Locate and identify every blood parasite.
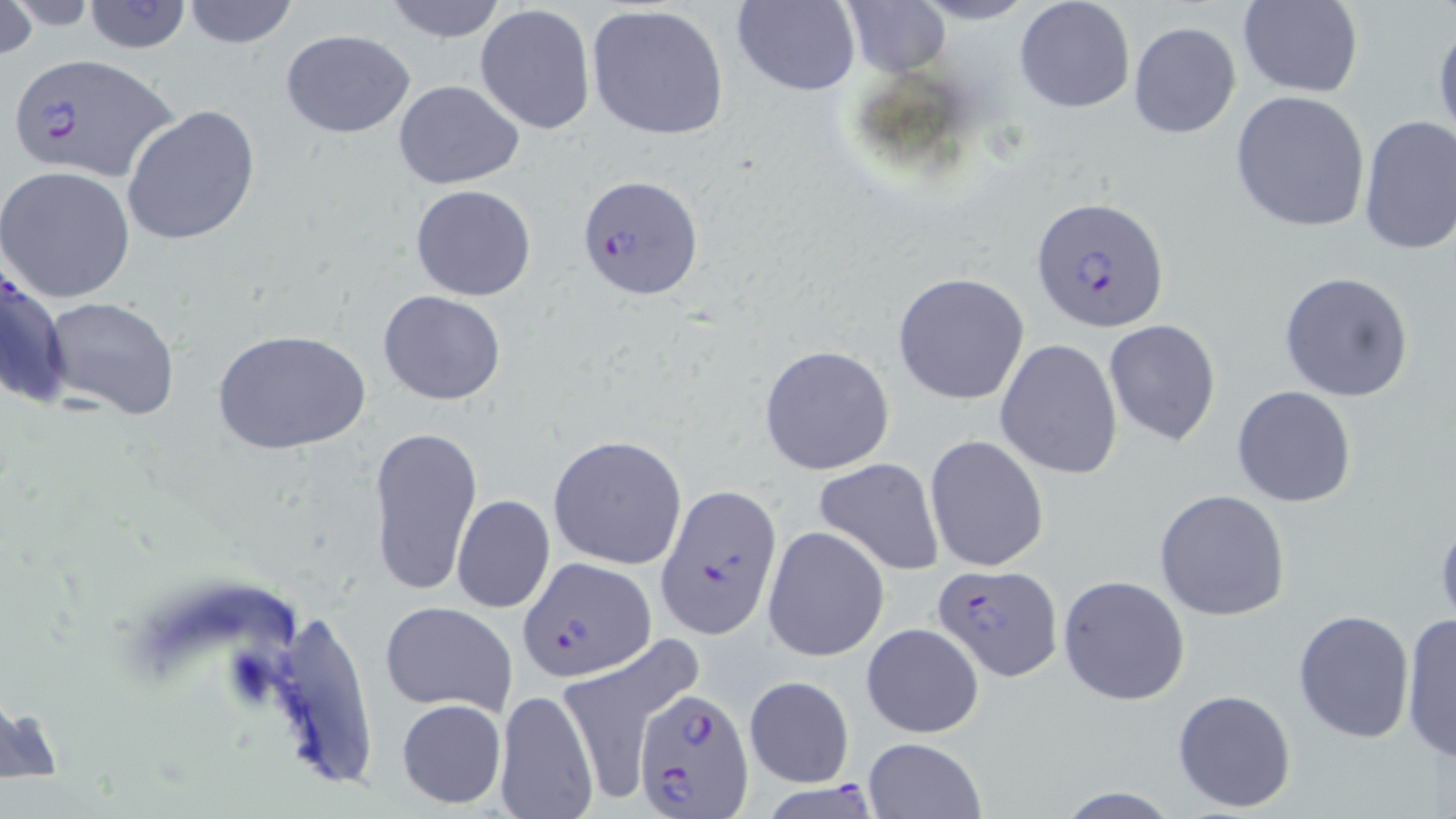

Approximate bounding boxes as named x1/y1/x2/y2 corners in pixels.
Plasmodium falciparum-infected red blood cells: (x1=9, y1=54, x2=181, y2=185), (x1=577, y1=174, x2=705, y2=302), (x1=1032, y1=196, x2=1170, y2=332), (x1=657, y1=487, x2=781, y2=640), (x1=519, y1=557, x2=656, y2=681), (x1=933, y1=563, x2=1062, y2=679), (x1=635, y1=687, x2=756, y2=819), (x1=765, y1=775, x2=877, y2=819).
No Plasmodium ovale, Plasmodium malariae, Plasmodium vivax, Babesia divergens, or Trypanosoma brucei observed.

Uninfected red blood cell locations: (x1=0, y1=0, x2=37, y2=63), (x1=383, y1=0, x2=508, y2=44), (x1=732, y1=0, x2=858, y2=95), (x1=1014, y1=0, x2=1136, y2=114), (x1=1237, y1=0, x2=1363, y2=98), (x1=82, y1=1, x2=193, y2=54), (x1=181, y1=1, x2=300, y2=50), (x1=838, y1=1, x2=950, y2=78), (x1=585, y1=4, x2=733, y2=141), (x1=475, y1=5, x2=596, y2=133), (x1=1432, y1=20, x2=1456, y2=146), (x1=1127, y1=22, x2=1241, y2=138), (x1=279, y1=28, x2=416, y2=138), (x1=394, y1=79, x2=524, y2=190), (x1=1230, y1=89, x2=1371, y2=232), (x1=121, y1=106, x2=262, y2=248), (x1=1357, y1=115, x2=1456, y2=255), (x1=1, y1=165, x2=135, y2=304), (x1=409, y1=184, x2=538, y2=302), (x1=0, y1=258, x2=72, y2=411), (x1=1279, y1=271, x2=1414, y2=402), (x1=892, y1=272, x2=1030, y2=405), (x1=377, y1=290, x2=507, y2=405), (x1=42, y1=296, x2=182, y2=421), (x1=1104, y1=319, x2=1221, y2=447), (x1=211, y1=329, x2=372, y2=455), (x1=996, y1=339, x2=1124, y2=480), (x1=758, y1=344, x2=896, y2=475), (x1=1231, y1=385, x2=1356, y2=507), (x1=366, y1=425, x2=482, y2=598), (x1=925, y1=434, x2=1048, y2=573), (x1=547, y1=435, x2=688, y2=570), (x1=813, y1=457, x2=944, y2=576), (x1=1154, y1=489, x2=1291, y2=621), (x1=451, y1=494, x2=555, y2=612), (x1=1434, y1=508, x2=1456, y2=628), (x1=763, y1=525, x2=890, y2=662), (x1=1057, y1=575, x2=1189, y2=706), (x1=379, y1=601, x2=517, y2=715), (x1=252, y1=605, x2=381, y2=797), (x1=1293, y1=609, x2=1415, y2=743), (x1=1399, y1=612, x2=1456, y2=764), (x1=861, y1=622, x2=985, y2=740), (x1=553, y1=642, x2=700, y2=797), (x1=742, y1=676, x2=855, y2=787), (x1=493, y1=687, x2=601, y2=818), (x1=1171, y1=688, x2=1297, y2=813), (x1=396, y1=698, x2=508, y2=810), (x1=862, y1=737, x2=986, y2=819), (x1=1051, y1=786, x2=1186, y2=818). Slide-level diagnosis: Plasmodium falciparum. Thin blood film. May-Grünwald-Giemsa stain. Single field of view. Captured at 1000x magnification. Light microscopy. Image is 1456×819 pixels.